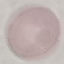 Result: no malaria parasites detected. Photographed with a smartphone camera at the microscope eyepiece. Automatically extracted cell patch, resized to 64 × 64 pixels. Giemsa-stained preparation. Thin blood film.